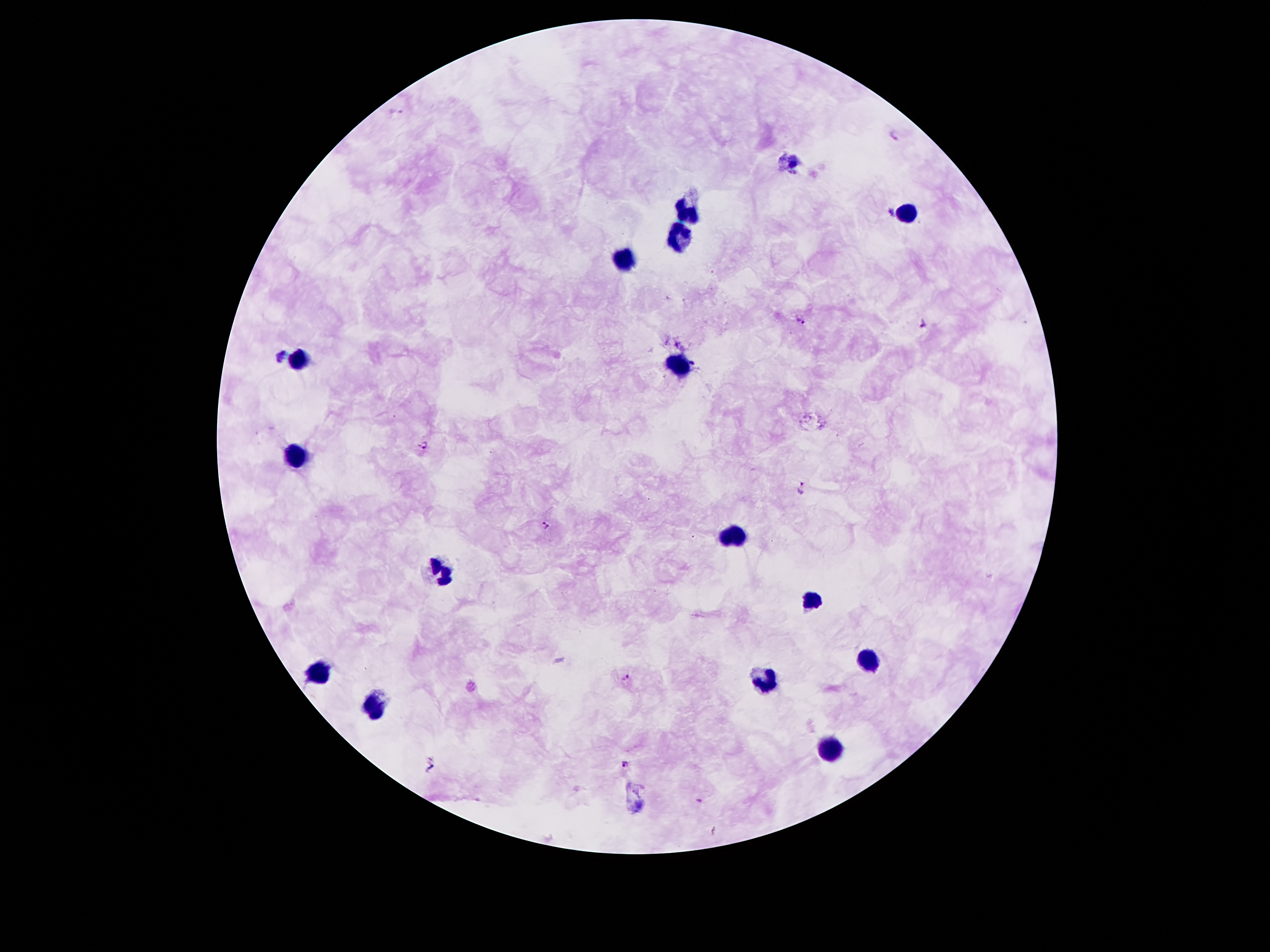

coordinate format = approximate object centers, in pixels from the top-left corner
leukocyte locations = (x=690, y=209), (x=908, y=214), (x=679, y=232), (x=624, y=261), (x=300, y=359), (x=676, y=366), (x=297, y=459), (x=735, y=534), (x=441, y=567), (x=817, y=601), (x=877, y=662), (x=322, y=670), (x=765, y=679), (x=372, y=703), (x=833, y=750)
malaria parasite locations = (x=895, y=134), (x=803, y=319), (x=925, y=323), (x=424, y=445), (x=803, y=486), (x=546, y=524), (x=626, y=676), (x=627, y=762)
patient malaria status = positive for Plasmodium falciparum
magnification = 100x
stain = Giemsa
field of view = single
capture = smartphone through the microscope eyepiece
image size = 1270×952 pixels
preparation = thick peripheral-blood smear